Locate every malaria parasite.
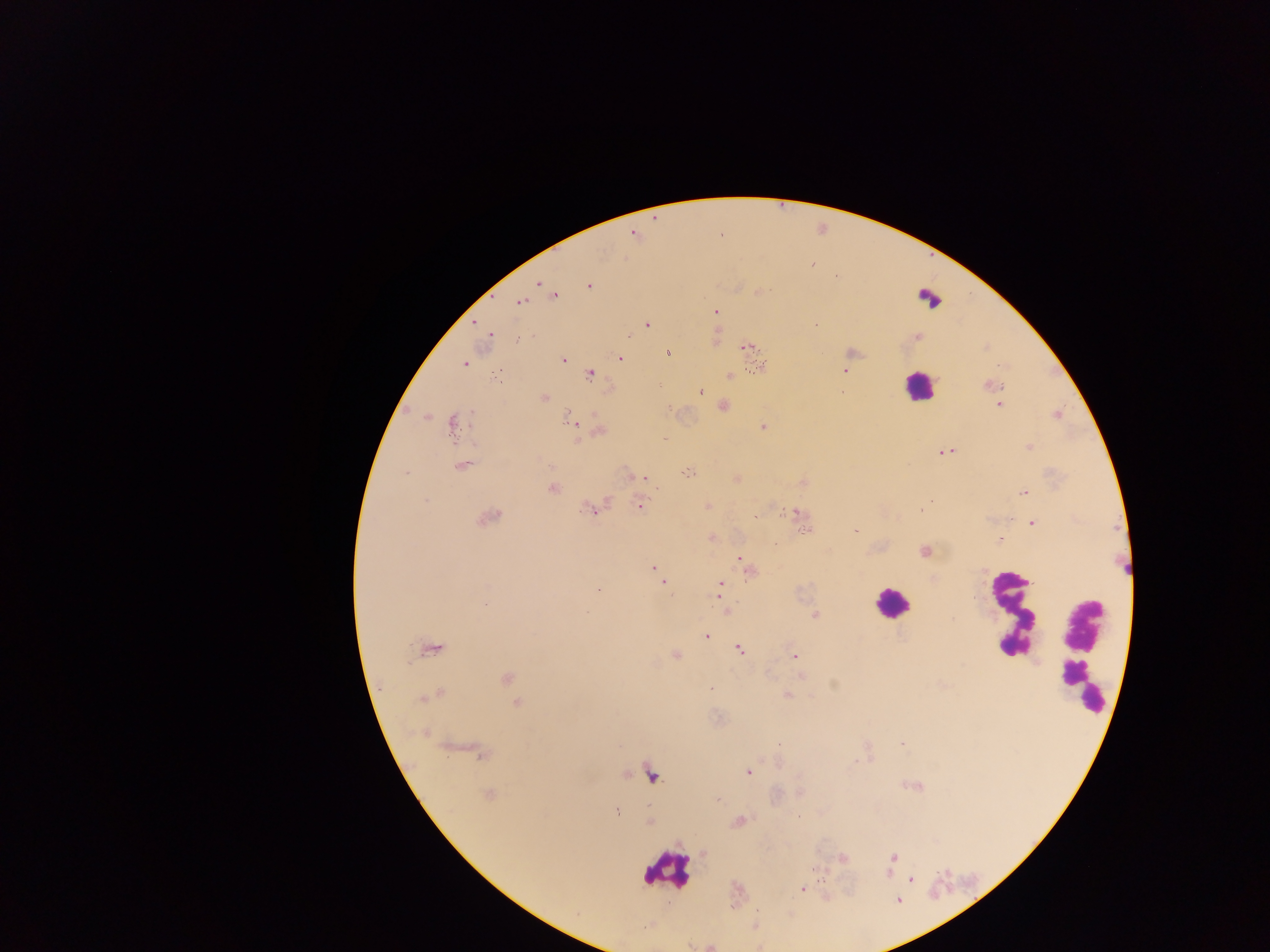
Approximate centers as [x, y] in pixels.
Malaria parasites: [630, 233], [813, 267], [535, 283], [757, 291], [555, 297], [519, 302], [718, 311], [646, 323], [489, 338], [520, 338], [916, 338], [716, 340], [745, 346], [668, 353], [621, 359], [563, 361], [464, 363], [846, 371], [589, 373], [496, 374], [729, 376], [998, 384], [990, 385], [701, 390], [543, 397], [999, 404], [723, 405], [569, 417], [763, 425], [451, 427], [577, 432], [597, 433], [663, 439], [1027, 448], [944, 449], [463, 465], [405, 471], [687, 473], [642, 477], [735, 479], [552, 488], [1023, 493], [426, 500], [707, 504], [597, 505], [639, 505], [921, 508], [783, 510], [797, 511], [755, 516], [488, 517], [1032, 522], [807, 529], [853, 529], [710, 537], [999, 538], [924, 550], [738, 558], [742, 562], [654, 567], [750, 572], [662, 582], [721, 584], [598, 589], [718, 596], [586, 614], [815, 614], [707, 637], [1001, 646], [435, 648], [739, 648], [1007, 650], [675, 656], [795, 656], [800, 675], [505, 678], [832, 684], [709, 688], [440, 692], [787, 694], [431, 695], [424, 698], [516, 703], [424, 734], [901, 743], [866, 747], [868, 753], [480, 755], [482, 757], [854, 761], [750, 771], [902, 785], [921, 787], [915, 788], [487, 795], [615, 810], [739, 819], [648, 820], [893, 858], [843, 859], [822, 877], [909, 879], [802, 889].

Summary:
  - Leukocyte locations: [913, 388], [895, 601], [1007, 611], [1082, 623], [1078, 688], [669, 874]
  - Preparation: thick blood smear
  - Country: Ghana
  - Field of view: single
  - Image size: 1270×952 pixels
  - Capture: mobile-phone photograph through a microscope